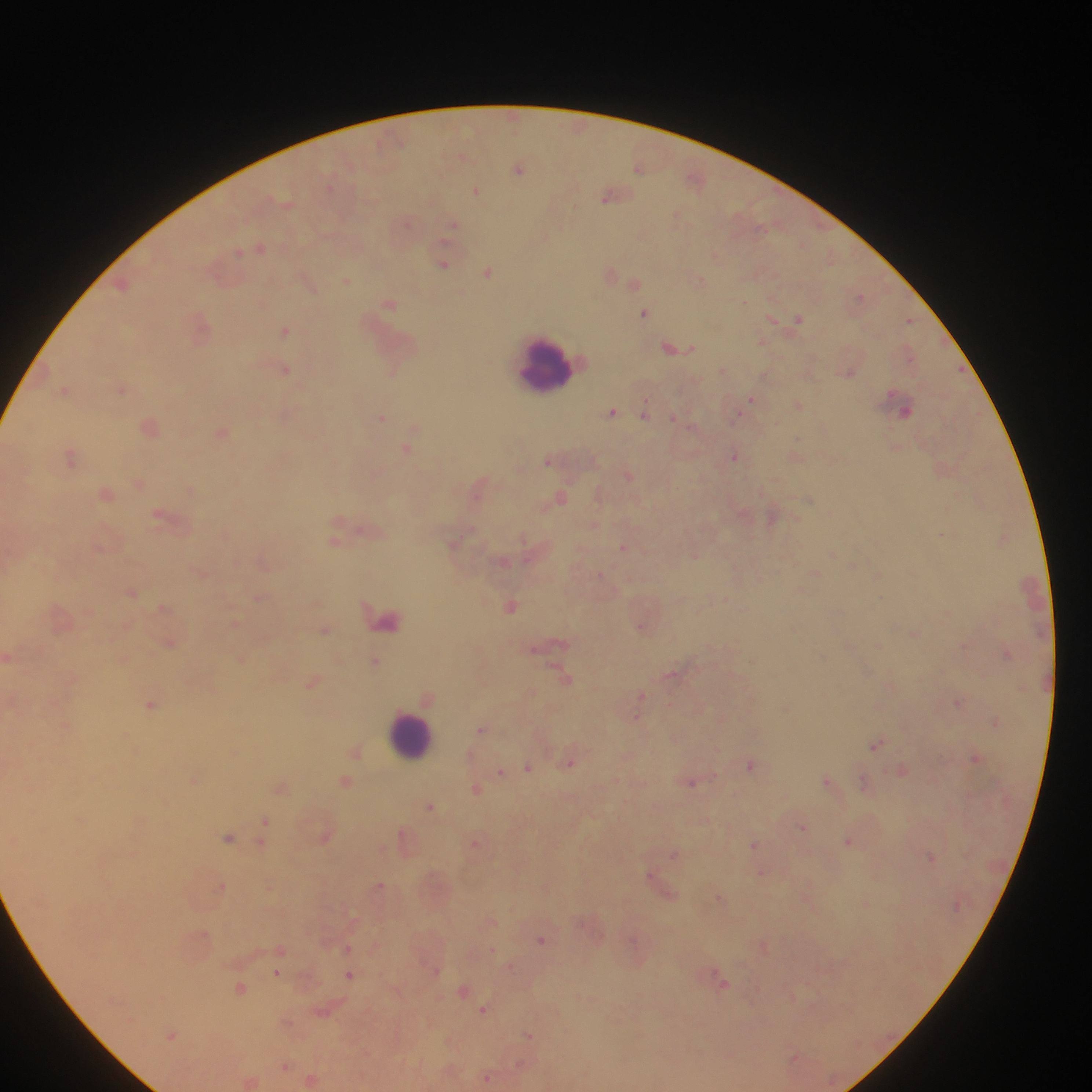
preparation = thick blood film
leukocyte locations = approximate centers as (x, y) in pixels: (548, 364), (411, 736)
malaria parasite locations = approximate centers as (x, y) in pixels: (462, 156), (639, 167), (519, 168), (695, 179), (476, 190), (612, 194), (407, 222), (452, 226), (261, 247), (444, 264), (489, 271), (610, 272), (700, 279), (346, 281), (634, 282), (860, 296), (388, 303), (645, 312), (798, 319), (910, 320), (201, 325), (286, 330), (676, 347), (909, 353), (284, 367), (724, 369), (848, 371), (122, 387), (65, 390), (751, 399), (799, 405), (901, 405), (612, 412), (645, 412), (381, 417), (676, 418), (151, 426), (222, 432), (407, 448), (735, 456), (72, 457), (550, 459), (629, 474), (140, 483), (480, 486), (191, 489), (106, 492), (599, 495), (561, 497), (809, 498), (167, 516), (772, 516), (225, 533), (336, 540), (454, 543), (624, 547), (695, 555), (263, 559), (503, 560), (201, 572), (815, 573), (133, 592), (260, 597), (726, 598), (511, 605), (164, 607), (387, 618), (642, 625), (325, 629), (913, 632), (169, 642), (552, 643), (965, 645), (1007, 653), (9, 656), (241, 658), (376, 660), (673, 674), (565, 676), (314, 682), (892, 684), (428, 696), (641, 696), (12, 698), (958, 702), (151, 705), (637, 715), (996, 721), (67, 725), (482, 729), (878, 744), (356, 751), (471, 755), (976, 757), (571, 761), (752, 763), (528, 767), (903, 769), (502, 772), (195, 779), (346, 781), (689, 782), (829, 782), (867, 784), (282, 788), (476, 788), (431, 805), (266, 821), (803, 827), (325, 836), (406, 836), (229, 837), (849, 840), (476, 842), (262, 843), (755, 844), (674, 854), (930, 856), (762, 872), (652, 877), (221, 884), (379, 885), (720, 897), (491, 920), (543, 939), (764, 947), (347, 948), (281, 949), (511, 966), (280, 969), (278, 972), (350, 974), (720, 979), (241, 987), (464, 989), (485, 1009), (324, 1010), (287, 1021), (172, 1034), (529, 1034), (795, 1056), (285, 1065), (488, 1078), (312, 1079), (250, 1080)
image size = 1092×1092 pixels
country = Ghana
field of view = single
capture = mobile-phone photograph through a microscope